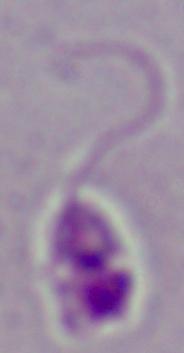
Captured at 1000x magnification. Photomicrograph. A Leishmania parasite is shown.